Locate every Plasmodium ovale-infected red blood cell.
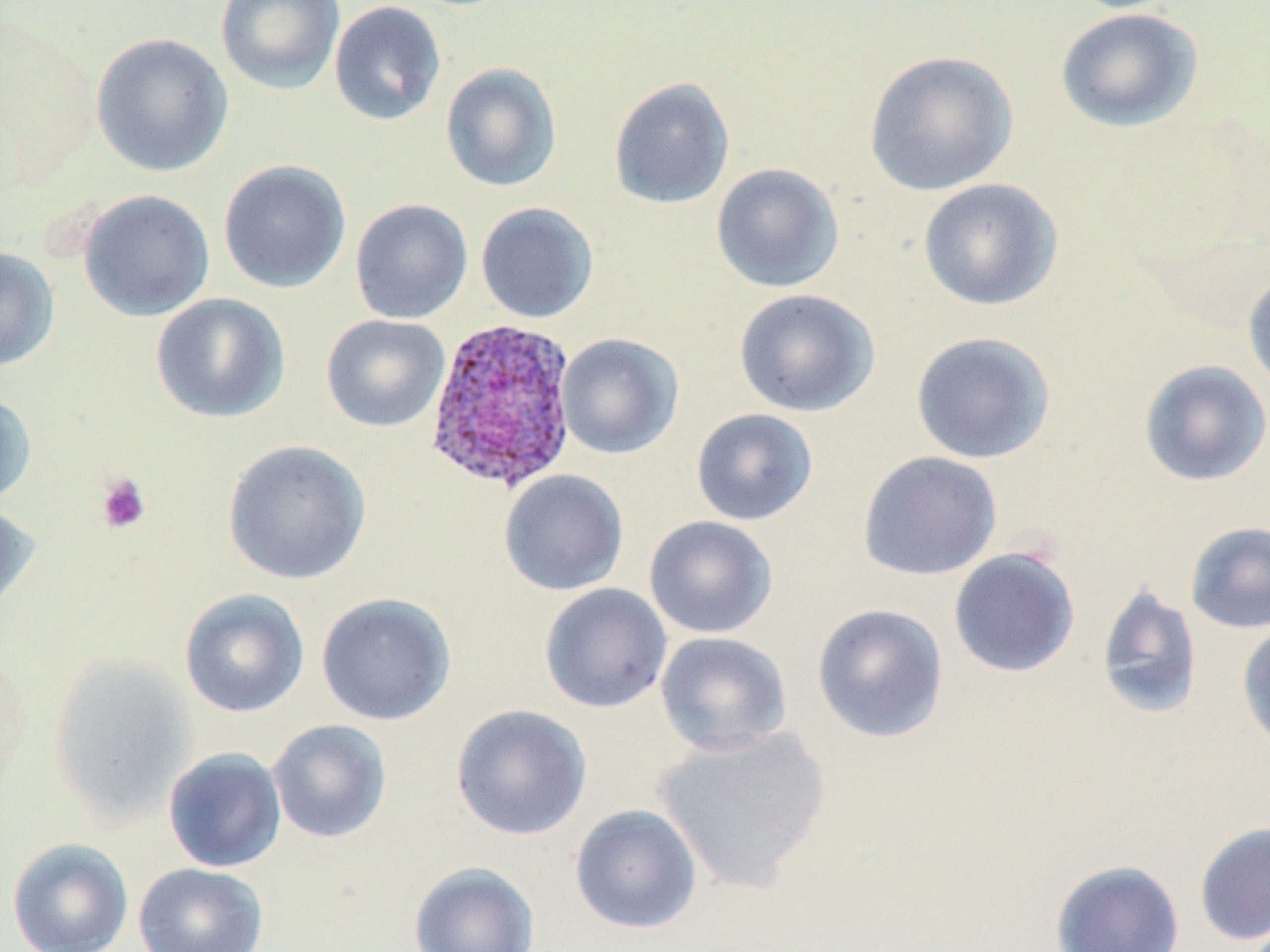

Approximate bounding boxes as (x1,y1)-(x2,y2) corner pairs in pixels.
Plasmodium ovale-infected red blood cells: (423,316)-(579,493).

Summary:
  - Platelet locations: (95,473)-(152,535)
  - Uninfected red blood cell locations: (215,0)-(345,95), (329,1)-(446,126), (1055,7)-(1203,133), (90,32)-(234,178), (864,50)-(1018,196), (440,63)-(562,192), (608,77)-(735,210), (218,159)-(352,294), (710,162)-(845,293), (917,177)-(1063,312), (77,189)-(215,322), (350,198)-(472,324), (475,202)-(599,323), (0,245)-(60,371), (1242,268)-(1270,397), (733,288)-(879,417), (150,293)-(291,423), (320,315)-(451,432), (910,331)-(1055,464), (556,333)-(683,459), (1138,359)-(1270,487), (0,392)-(37,508), (690,408)-(818,526), (221,439)-(372,585), (857,451)-(1002,581), (499,469)-(629,596), (0,500)-(39,621), (643,515)-(778,639), (1185,521)-(1270,634), (948,548)-(1081,678), (539,583)-(673,713), (1095,584)-(1203,720), (179,588)-(310,718), (316,592)-(456,726), (811,603)-(949,743), (1236,620)-(1270,753), (655,631)-(792,757), (47,654)-(197,823), (451,703)-(592,841), (267,718)-(392,843), (652,724)-(831,892), (162,747)-(287,872), (569,804)-(702,934), (1192,821)-(1270,946), (6,837)-(133,952), (1050,859)-(1185,952), (408,861)-(539,952), (133,862)-(269,952)
  - Slide-level diagnosis: Plasmodium ovale
  - Magnification: 1000x
  - Modality: optical microscopy
  - Preparation: thin blood smear
  - Stain: May-Grünwald-Giemsa
  - Image size: 1270×952 pixels
  - Field of view: single